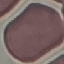
result = negative for malaria parasites
stain = Giemsa
preparation = thin blood smear
capture = smartphone through the microscope eyepiece
image type = automatically extracted cell patch, resized to 64 × 64 pixels